Comment on the morphology of the red blood cells.
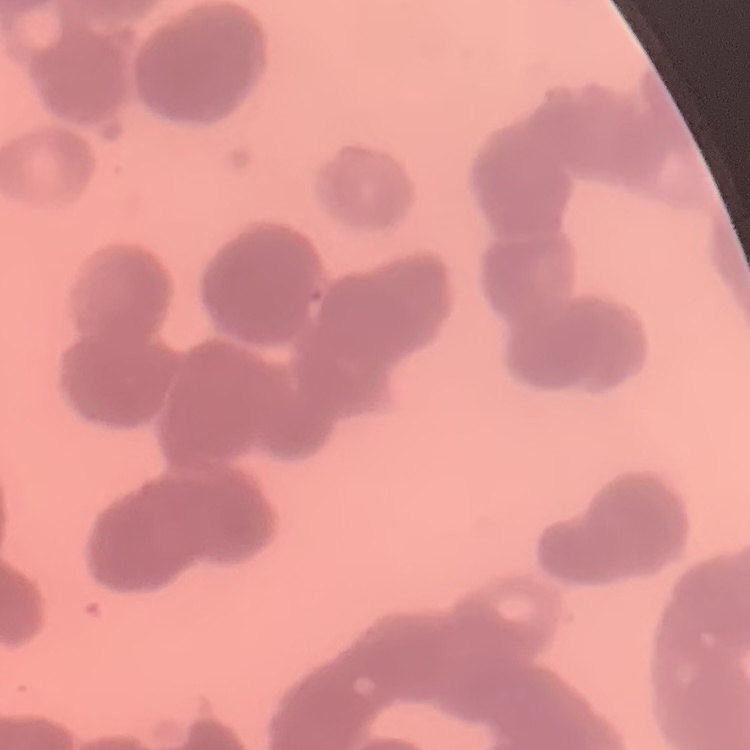
Rouleaux formation.

Summary:
  - Image type: one tile cut from a larger photomicrograph
  - Preparation: thin blood film
  - Stain: Field's or Giemsa